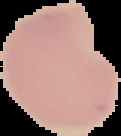
{
  "image_size": "121×136 pixels",
  "result": "negative for Plasmodium parasites",
  "image_type": "segmented cell region with the area outside set to black",
  "preparation": "thin blood smear"
}